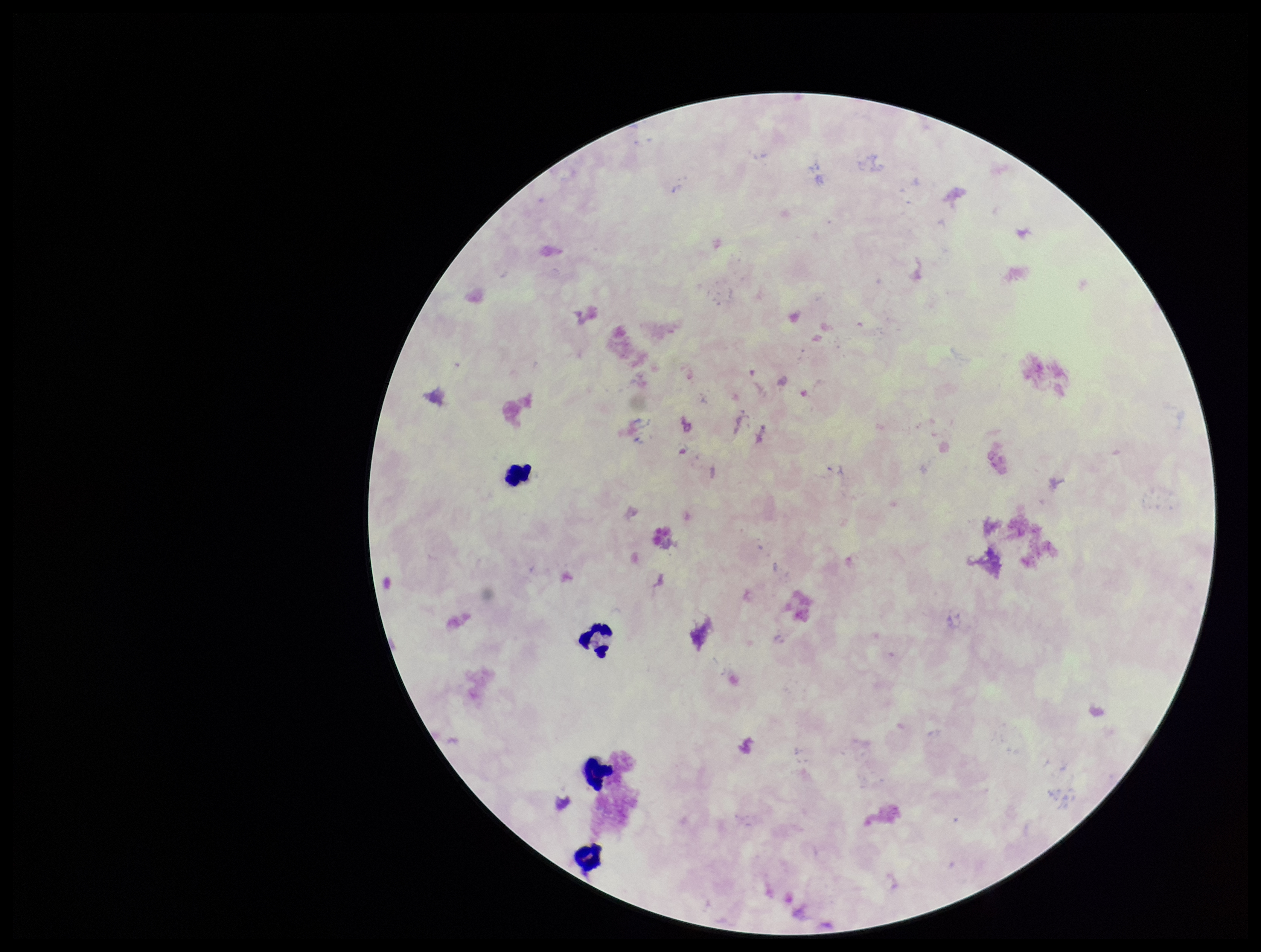
Patient malaria status: negative. Leukocyte count: 4. Stained with Giemsa. Parasite count: 0. Photographed through the microscope eyepiece with a smartphone camera. Image is 1261×952 pixels. Preparation: thick blood smear. Single field of view. Plasmodium parasites: none identified.